Locate every Plasmodium falciparum-infected red blood cell.
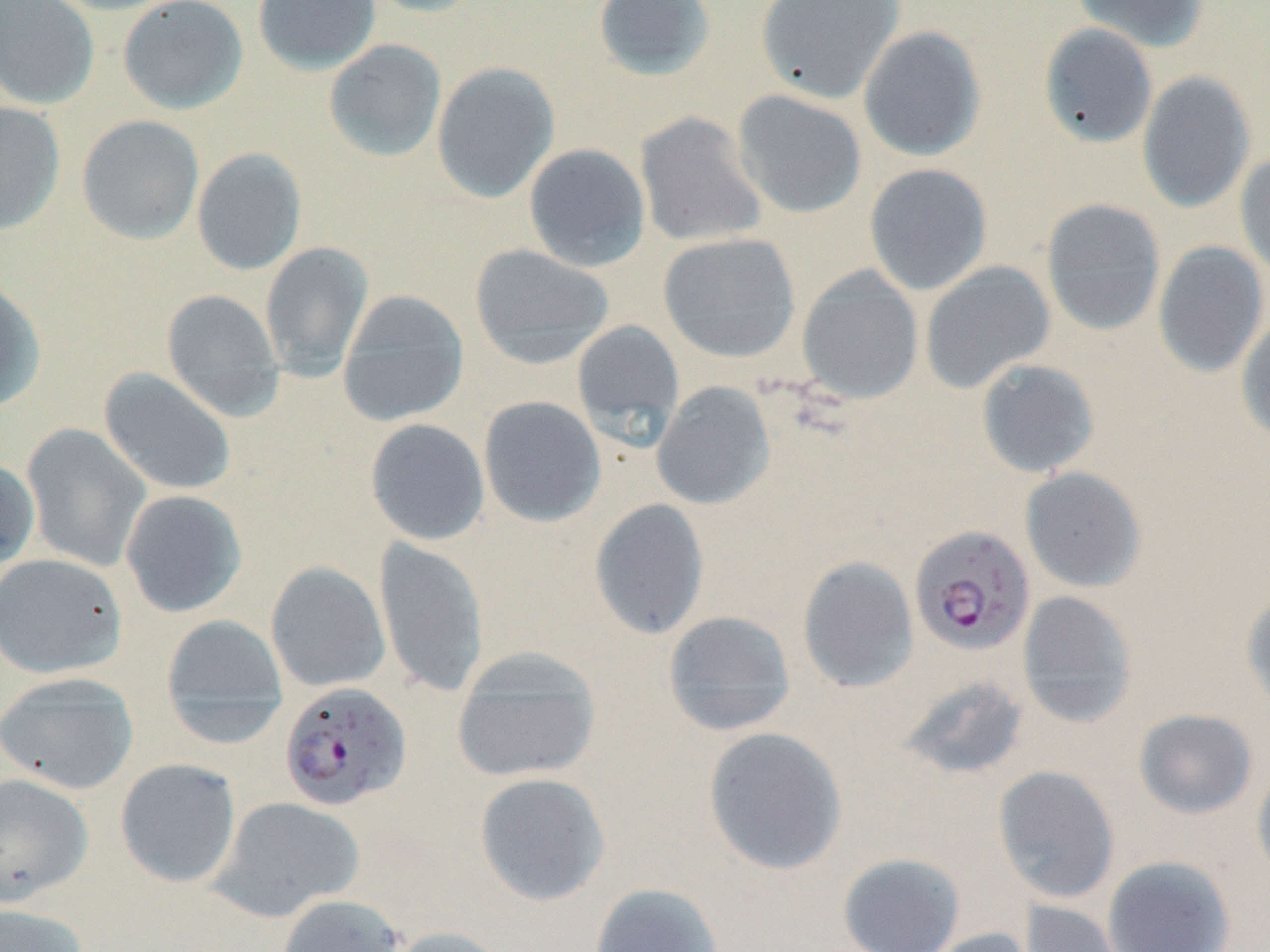
Approximate bounding boxes as named x1/y1/x2/y2 corners in pixels.
Plasmodium falciparum-infected red blood cells: (x1=909, y1=525, x2=1035, y2=656), (x1=278, y1=682, x2=412, y2=811).

Summary:
  - Uninfected red blood cell locations: (x1=0, y1=0, x2=101, y2=110), (x1=45, y1=0, x2=186, y2=15), (x1=117, y1=0, x2=249, y2=115), (x1=252, y1=0, x2=381, y2=75), (x1=361, y1=0, x2=489, y2=18), (x1=592, y1=0, x2=716, y2=80), (x1=755, y1=0, x2=905, y2=104), (x1=1070, y1=0, x2=1208, y2=52), (x1=1039, y1=23, x2=1158, y2=148), (x1=858, y1=25, x2=987, y2=161), (x1=323, y1=38, x2=447, y2=162), (x1=431, y1=62, x2=560, y2=203), (x1=1137, y1=71, x2=1256, y2=213), (x1=731, y1=89, x2=867, y2=219), (x1=0, y1=101, x2=66, y2=235), (x1=634, y1=112, x2=768, y2=248), (x1=76, y1=115, x2=205, y2=246), (x1=523, y1=143, x2=651, y2=272), (x1=192, y1=147, x2=307, y2=275), (x1=1234, y1=150, x2=1270, y2=281), (x1=864, y1=163, x2=992, y2=296), (x1=1040, y1=199, x2=1166, y2=336), (x1=658, y1=232, x2=801, y2=363), (x1=1152, y1=241, x2=1268, y2=378), (x1=259, y1=242, x2=374, y2=381), (x1=469, y1=243, x2=614, y2=369), (x1=919, y1=261, x2=1056, y2=394), (x1=796, y1=265, x2=924, y2=404), (x1=0, y1=275, x2=46, y2=412), (x1=160, y1=289, x2=286, y2=421), (x1=337, y1=289, x2=469, y2=427), (x1=1236, y1=312, x2=1270, y2=445), (x1=571, y1=320, x2=685, y2=445), (x1=976, y1=358, x2=1100, y2=478), (x1=98, y1=367, x2=236, y2=496), (x1=651, y1=381, x2=776, y2=510), (x1=478, y1=395, x2=607, y2=527), (x1=365, y1=418, x2=490, y2=546), (x1=21, y1=423, x2=151, y2=572), (x1=0, y1=458, x2=40, y2=571), (x1=1020, y1=466, x2=1147, y2=593), (x1=119, y1=489, x2=248, y2=618), (x1=589, y1=498, x2=710, y2=640), (x1=375, y1=538, x2=489, y2=697), (x1=0, y1=552, x2=127, y2=679), (x1=797, y1=556, x2=919, y2=694), (x1=265, y1=561, x2=390, y2=693), (x1=1240, y1=588, x2=1270, y2=713), (x1=1017, y1=591, x2=1138, y2=727), (x1=662, y1=610, x2=797, y2=736), (x1=159, y1=613, x2=289, y2=743), (x1=452, y1=649, x2=603, y2=782), (x1=0, y1=672, x2=139, y2=794), (x1=893, y1=675, x2=1032, y2=782), (x1=1133, y1=708, x2=1258, y2=820), (x1=701, y1=726, x2=848, y2=876), (x1=115, y1=758, x2=242, y2=887), (x1=1252, y1=761, x2=1270, y2=887), (x1=993, y1=765, x2=1121, y2=904), (x1=474, y1=772, x2=611, y2=906), (x1=0, y1=773, x2=94, y2=905), (x1=208, y1=796, x2=364, y2=922), (x1=837, y1=851, x2=966, y2=952), (x1=1103, y1=855, x2=1236, y2=952), (x1=589, y1=883, x2=726, y2=952), (x1=275, y1=893, x2=406, y2=952), (x1=1021, y1=900, x2=1129, y2=952), (x1=0, y1=903, x2=88, y2=952), (x1=386, y1=925, x2=513, y2=952), (x1=917, y1=927, x2=1039, y2=952)
  - Slide-level diagnosis: Plasmodium falciparum
  - Preparation: thin blood film
  - Field of view: single
  - Stain: May-Grünwald-Giemsa
  - Image size: 1270×952 pixels
  - Modality: light microscopy
  - Magnification: 1000x